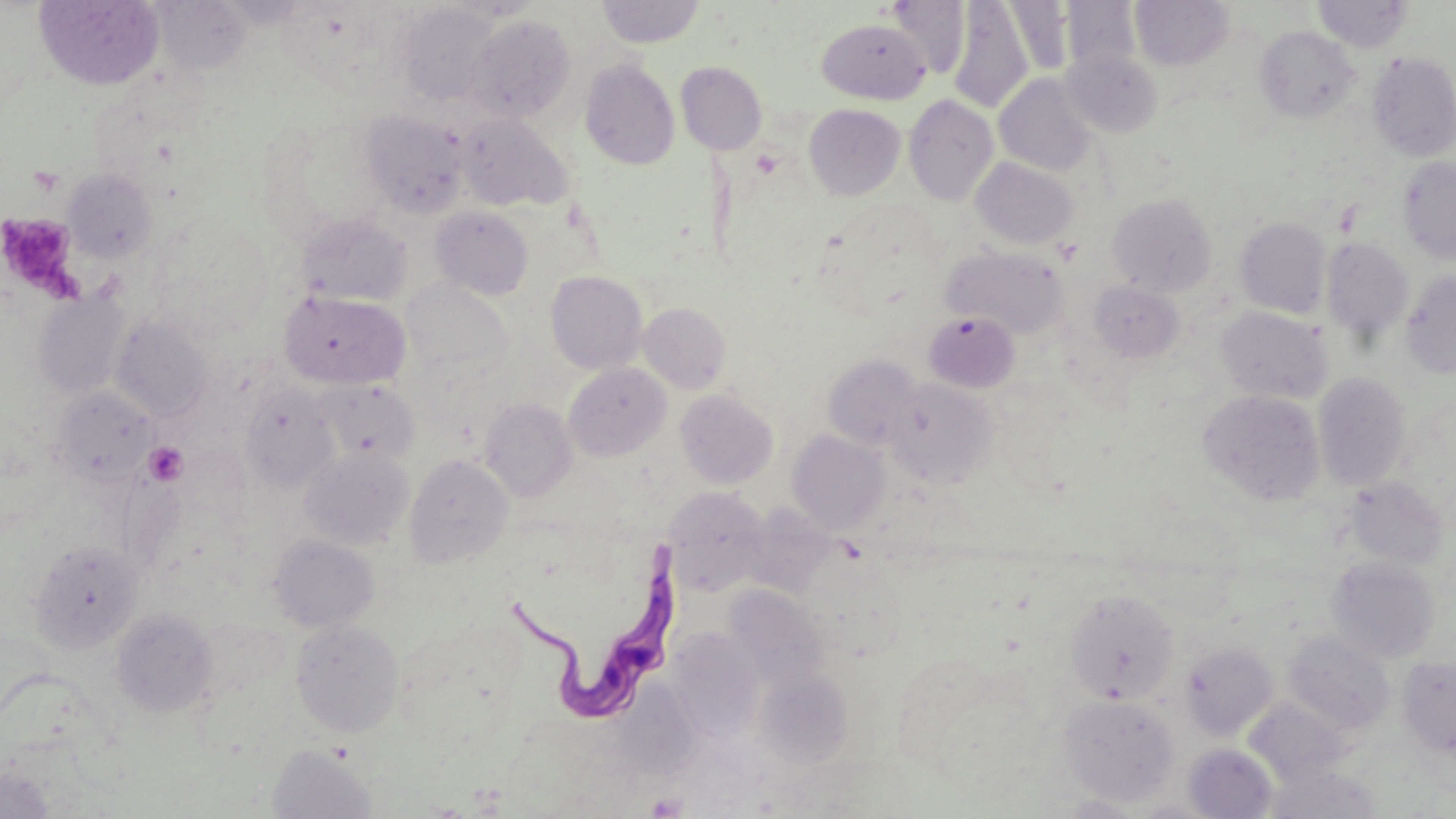
Summary:
  - Coordinate format: approximate bounding boxes as (x1,y1)-(x2,y2) corner pairs in pixels
  - Trypanosoma brucei locations: (507,538)-(680,725)
  - Uninfected red blood cell locations: (34,0)-(165,90), (595,0)-(707,48), (1130,0)-(1235,70), (1313,0)-(1413,53), (884,1)-(972,78), (948,1)-(1034,113), (1002,1)-(1074,78), (1059,1)-(1142,76), (151,2)-(252,75), (397,3)-(502,107), (467,15)-(576,122), (816,17)-(931,104), (1255,26)-(1361,124), (1062,49)-(1163,137), (1368,53)-(1456,161), (580,60)-(680,169), (675,61)-(767,155), (994,74)-(1098,176), (904,94)-(999,206), (804,104)-(906,200), (360,110)-(470,218), (455,114)-(572,211), (1398,156)-(1456,264), (970,157)-(1079,249), (63,168)-(158,263), (1107,193)-(1217,296), (430,207)-(534,300), (297,213)-(412,308), (150,216)-(274,341), (1234,217)-(1331,319), (1321,237)-(1414,345), (942,246)-(1069,339), (1400,270)-(1456,378), (545,271)-(648,374), (401,279)-(514,385), (1088,280)-(1184,364), (34,291)-(129,400), (279,291)-(411,389), (638,302)-(732,393), (1216,307)-(1333,404), (923,310)-(1020,393), (111,315)-(212,421), (822,354)-(924,451), (563,363)-(672,462), (1313,373)-(1412,490), (883,377)-(999,488), (317,379)-(420,463), (240,383)-(340,492), (51,386)-(156,486), (675,389)-(778,489), (1201,391)-(1326,506), (479,398)-(578,502), (787,430)-(890,535), (300,446)-(415,550), (404,453)-(514,569), (1341,475)-(1449,571), (664,487)-(771,595), (268,535)-(379,632), (30,540)-(144,653), (1327,557)-(1440,663), (724,584)-(830,690), (1063,588)-(1181,705), (111,609)-(218,718), (290,619)-(405,737), (668,628)-(766,744), (1284,631)-(1395,736), (1181,642)-(1279,741), (1397,655)-(1456,760), (754,667)-(853,768), (1057,695)-(1179,806), (1244,698)-(1350,785), (268,743)-(378,818), (1183,743)-(1279,818), (1262,764)-(1384,818), (0,767)-(56,818), (1052,793)-(1153,818)
  - Platelet locations: (28,165)-(64,197), (0,213)-(84,302), (143,441)-(189,487), (645,791)-(689,818)
  - Slide-level diagnosis: Trypanosoma brucei
  - Magnification: 1000x
  - Image size: 1456×819 pixels
  - Modality: light microscopy
  - Preparation: thin blood film
  - Field of view: single
  - Stain: May-Grünwald-Giemsa